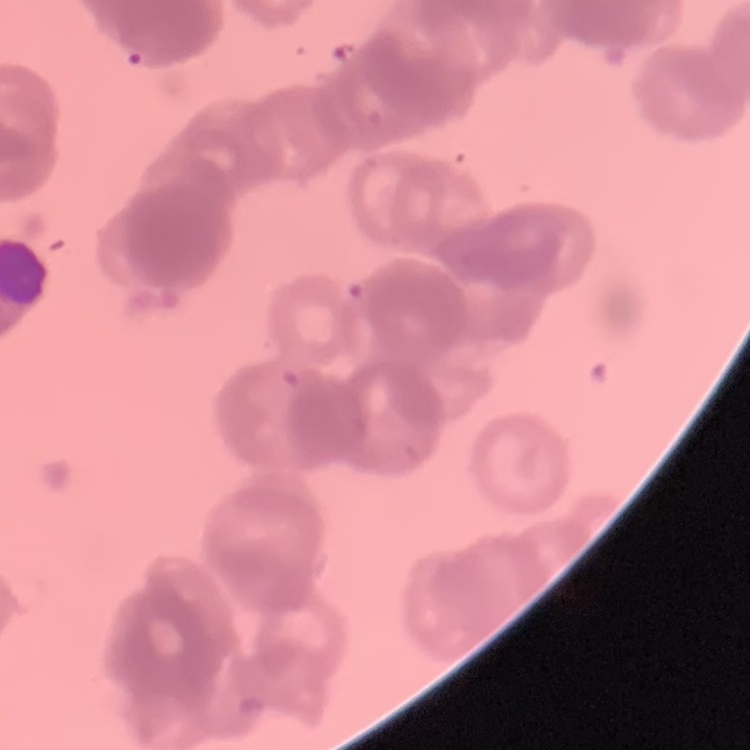

Summary:
  - Erythrocyte morphology: rouleaux formation
  - Image type: one tile cut from a larger photomicrograph
  - Preparation: thin blood smear
  - Stain: Field's or Giemsa